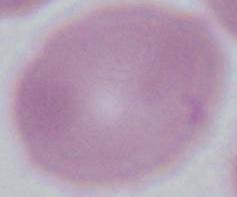
Summary:
  - Magnification: 1000x
  - Identification: red blood cell
  - Modality: photomicrograph